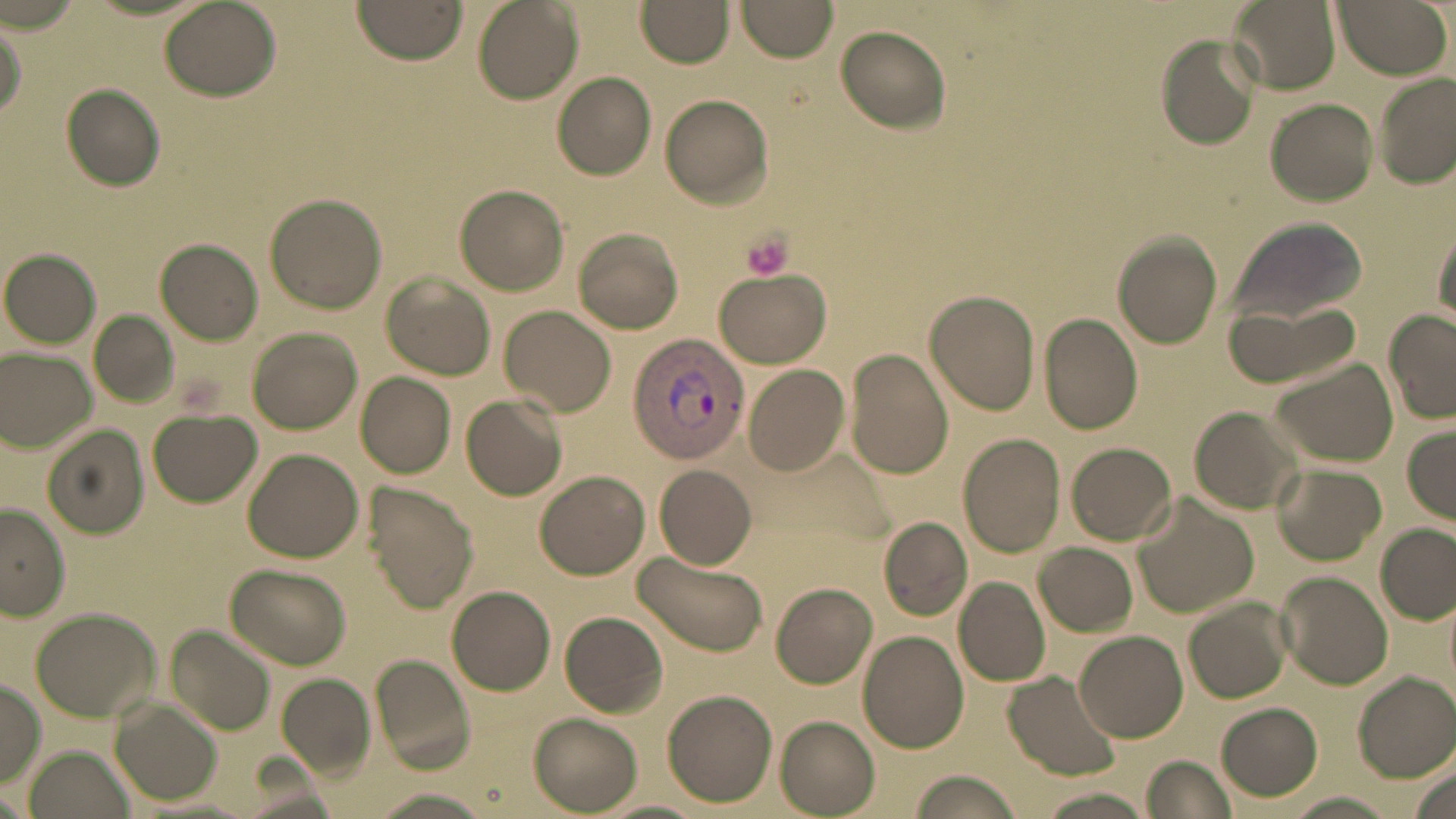
Summary:
  - Coordinate format: approximate bounding boxes as (x1, y1, x2, y2) in pixels
  - Plasmodium vivax-infected red blood cell locations: (627, 330, 750, 465)
  - Uninfected red blood cell locations: (736, 0, 839, 62), (1227, 0, 1340, 94), (1330, 0, 1451, 77), (160, 1, 280, 101), (351, 1, 467, 67), (473, 1, 583, 104), (636, 1, 735, 67), (1, 14, 27, 125), (835, 27, 952, 133), (1155, 35, 1260, 149), (1374, 72, 1454, 189), (553, 73, 657, 180), (61, 84, 167, 190), (660, 96, 775, 207), (1264, 98, 1377, 206), (454, 184, 569, 294), (265, 192, 387, 314), (1228, 217, 1368, 327), (1431, 220, 1455, 329), (573, 229, 684, 332), (1110, 232, 1224, 349), (154, 239, 262, 345), (1, 250, 100, 348), (711, 271, 831, 368), (382, 273, 495, 381), (924, 289, 1041, 415), (1225, 300, 1365, 388), (502, 305, 616, 416), (89, 311, 177, 406), (1383, 311, 1456, 424), (1037, 312, 1144, 435), (247, 327, 362, 434), (2, 348, 96, 450), (844, 348, 954, 479), (1270, 360, 1397, 467), (744, 362, 852, 477), (355, 371, 455, 479), (460, 394, 567, 501), (1190, 406, 1303, 513), (149, 409, 261, 507), (44, 422, 151, 537), (1402, 424, 1456, 522), (957, 434, 1065, 556), (1067, 442, 1176, 544), (242, 448, 365, 562), (1274, 462, 1385, 564), (653, 465, 757, 570), (533, 470, 649, 581), (367, 483, 478, 612), (1132, 491, 1258, 620), (0, 502, 69, 622), (879, 515, 973, 620), (1375, 524, 1454, 625), (1033, 542, 1137, 636), (632, 548, 769, 658), (227, 563, 350, 669), (1277, 572, 1392, 689), (954, 578, 1050, 688), (772, 582, 878, 689), (447, 585, 557, 694), (1184, 598, 1292, 703), (30, 608, 160, 723), (560, 611, 668, 718), (167, 626, 276, 734), (857, 631, 970, 753), (1076, 631, 1187, 741), (371, 654, 475, 770), (1004, 670, 1124, 781), (276, 672, 376, 778), (1353, 673, 1456, 781), (0, 679, 45, 784), (662, 689, 778, 806), (111, 700, 221, 806), (1215, 703, 1322, 799), (527, 712, 641, 814), (774, 715, 881, 815), (29, 747, 130, 819), (1141, 756, 1234, 819), (1404, 764, 1456, 819), (906, 770, 1022, 819), (1031, 788, 1156, 819), (368, 790, 495, 819), (1280, 793, 1398, 819)
  - Platelet locations: (740, 229, 794, 282)
  - Slide-level diagnosis: Plasmodium vivax
  - Preparation: thin blood film
  - Stain: May-Grünwald-Giemsa
  - Modality: light microscopy
  - Magnification: 1000x
  - Image size: 1456×819 pixels
  - Field of view: single